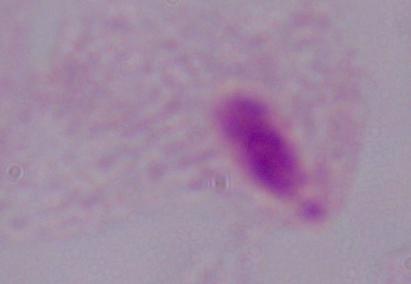
Captured at 1000x magnification. Micrograph. A trichomonad is seen.